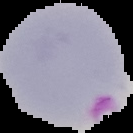

From a thin blood film. Malaria status: parasitized. The area outside the segmented cell region is set to black. Image is 133×133 pixels.